Locate every leukocyte (white blood cell).
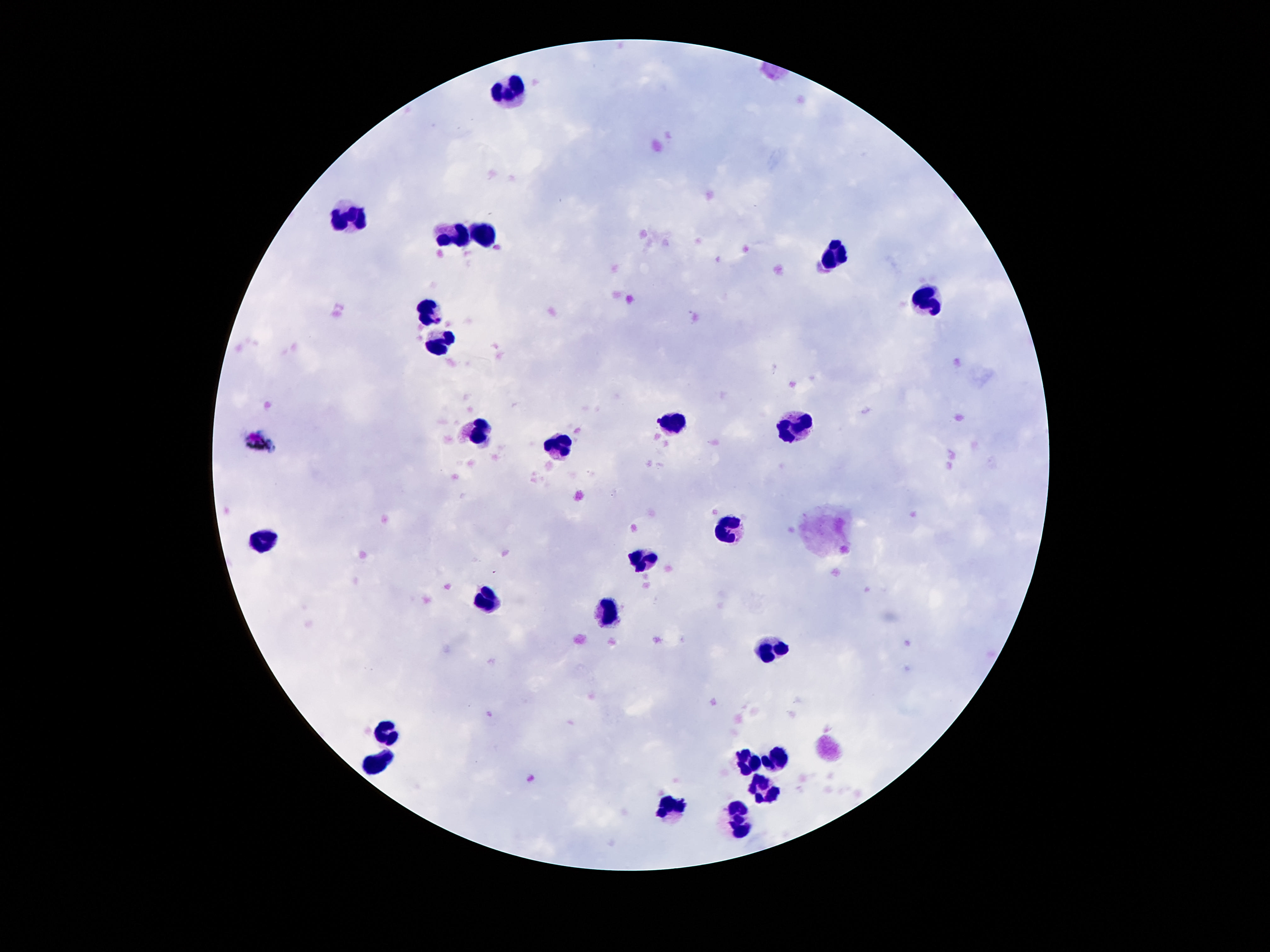

Approximate centers as {x, y} in pixels.
Leukocytes: {509, 92}, {347, 212}, {446, 231}, {486, 232}, {837, 255}, {933, 300}, {433, 313}, {444, 342}, {673, 422}, {475, 430}, {799, 430}, {557, 446}, {725, 530}, {267, 539}, {643, 562}, {482, 597}, {608, 619}, {769, 647}, {387, 730}, {778, 758}, {377, 763}, {746, 763}, {763, 789}, {671, 810}, {740, 824}.

Patient malaria status: negative. Photographed through the microscope eyepiece with a smartphone camera. Giemsa-stained preparation. Thick blood film. 100x magnification. Image is 1270×952 pixels. One field from this slide.